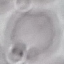 Result: no malaria parasites detected. Cell patch, automatically extracted from a larger field of view and resized to 64 × 64 pixels. Giemsa-stained preparation. Acquired by smartphone through the microscope eyepiece. Thin blood smear.